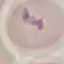

{
  "malaria_status": "uninfected",
  "capture": "smartphone through the microscope eyepiece",
  "image_type": "cell patch, automatically extracted from a larger field of view and resized to 64 × 64 pixels",
  "preparation": "thin smear",
  "stain": "Giemsa"
}